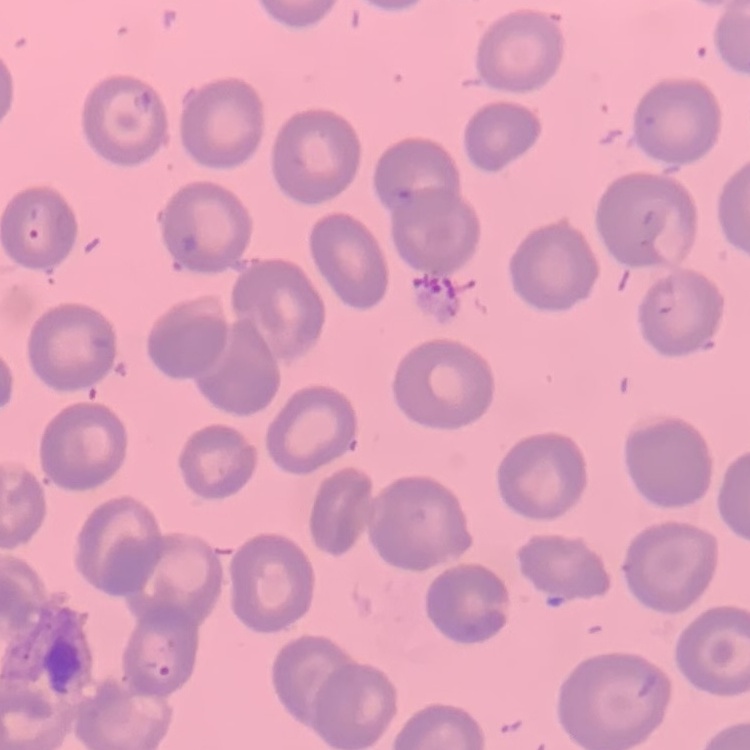
The erythrocytes exhibit no rouleaux formation. Stained with either Field's or Giemsa. One tile cut from a larger photomicrograph. Thin peripheral smear.